Locate and identify every blood parasite.
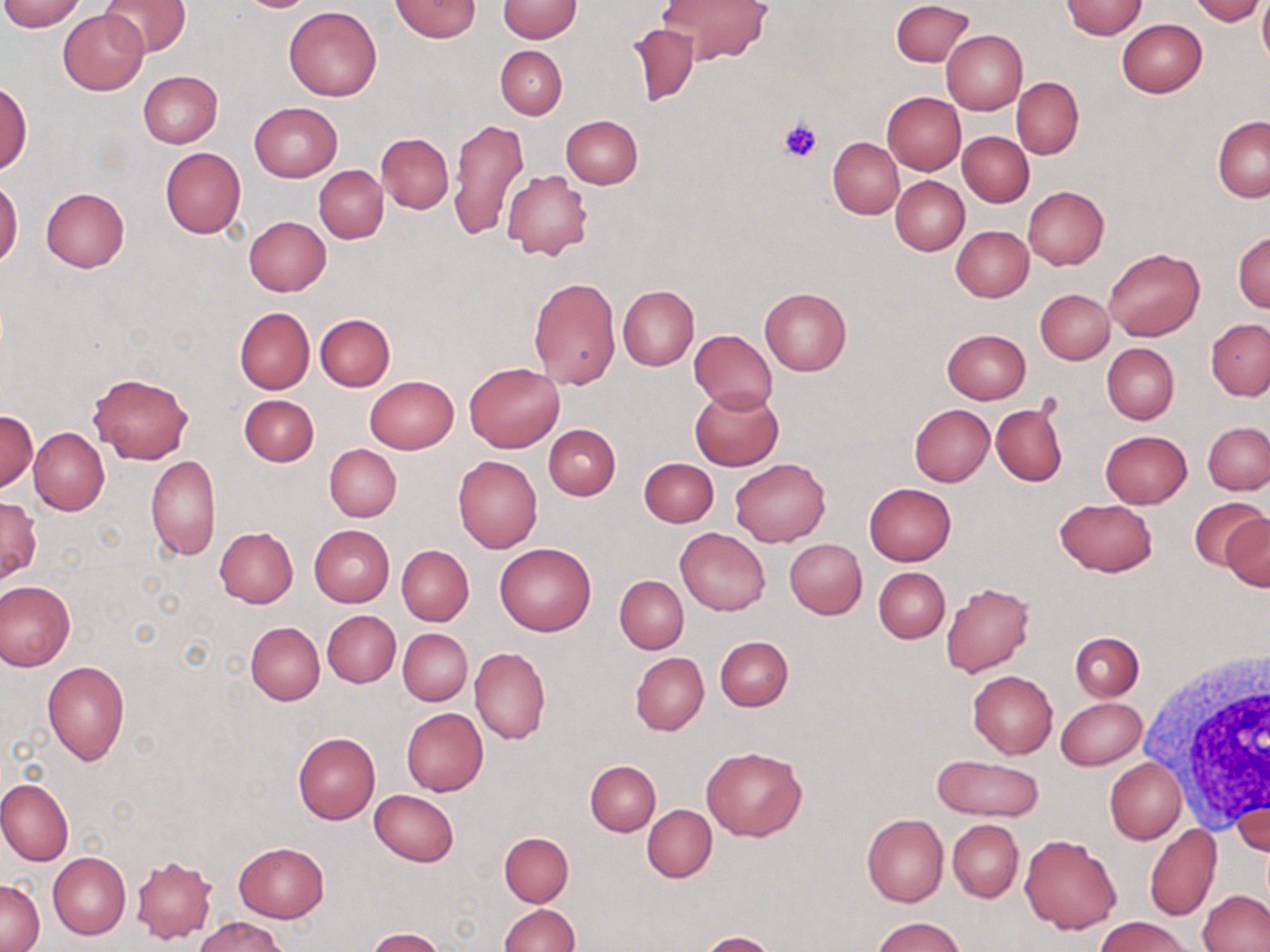

No blood parasites seen.

Approximate bounding boxes as [x1, y1, x2, y2] in pixels. White blood cell locations: [1135, 648, 1270, 840]. Uninfected red blood cell locations: [0, 0, 86, 31], [99, 0, 191, 59], [391, 0, 481, 42], [498, 0, 581, 42], [660, 0, 770, 64], [892, 0, 973, 67], [1061, 0, 1147, 39], [1190, 0, 1264, 24], [1258, 0, 1270, 67], [284, 6, 382, 101], [59, 9, 148, 94], [1117, 19, 1206, 97], [626, 23, 700, 107], [942, 30, 1028, 115], [496, 46, 567, 119], [138, 71, 223, 148], [1012, 76, 1084, 159], [1, 83, 32, 173], [882, 91, 966, 174], [249, 102, 343, 182], [560, 115, 642, 189], [1212, 116, 1270, 201], [448, 118, 530, 241], [957, 131, 1034, 207], [377, 132, 453, 213], [829, 138, 904, 219], [160, 147, 245, 239], [315, 165, 388, 243], [502, 170, 593, 261], [891, 176, 969, 255], [0, 179, 23, 267], [1023, 185, 1108, 270], [40, 186, 129, 273], [243, 216, 330, 296], [950, 225, 1034, 301], [1233, 232, 1270, 313], [1104, 246, 1204, 341], [529, 277, 621, 388], [617, 285, 699, 371], [760, 288, 852, 376], [1036, 289, 1114, 364], [234, 307, 314, 393], [315, 314, 395, 392], [1206, 319, 1270, 400], [941, 328, 1031, 404], [689, 330, 777, 412], [1101, 343, 1178, 424], [464, 362, 564, 452], [89, 372, 192, 463], [365, 375, 458, 453], [689, 388, 783, 471], [239, 394, 318, 467], [909, 403, 995, 486], [991, 403, 1067, 486], [1, 411, 37, 491], [1203, 421, 1270, 494], [544, 424, 621, 500], [29, 428, 109, 515], [1100, 430, 1193, 508], [324, 444, 401, 521], [147, 455, 221, 560], [453, 455, 542, 553], [639, 457, 718, 527], [730, 459, 831, 547], [864, 482, 955, 565], [0, 496, 42, 583], [1188, 497, 1266, 577], [1054, 499, 1157, 576], [1222, 512, 1270, 591], [309, 525, 395, 607], [214, 527, 298, 607], [675, 528, 769, 616], [786, 539, 866, 618], [494, 542, 596, 636], [397, 545, 474, 625], [873, 566, 949, 642], [615, 575, 688, 654], [0, 581, 75, 670], [942, 582, 1034, 678], [322, 610, 400, 687], [245, 622, 324, 705], [398, 629, 471, 705], [1070, 632, 1143, 701], [716, 635, 793, 710], [470, 648, 550, 744], [630, 652, 709, 735], [42, 660, 130, 767], [968, 669, 1057, 758], [951, 673, 1047, 823], [1055, 696, 1146, 770], [401, 708, 489, 796], [293, 732, 380, 824], [702, 746, 806, 840], [931, 754, 1044, 821], [1105, 757, 1186, 844], [585, 760, 661, 835], [0, 778, 73, 865], [370, 790, 458, 867], [1232, 794, 1269, 858], [642, 806, 716, 882], [862, 813, 948, 906], [949, 819, 1023, 902], [1144, 823, 1221, 920], [499, 832, 573, 906], [1019, 834, 1121, 934], [234, 842, 329, 923], [48, 852, 130, 939], [131, 854, 218, 943], [1, 877, 43, 951], [1199, 890, 1270, 951], [499, 904, 578, 952], [1097, 915, 1192, 951], [195, 916, 287, 952], [874, 917, 965, 952], [366, 928, 445, 952], [700, 931, 776, 952]. Platelet locations: [779, 116, 824, 161]. Slide-level diagnosis: negative for blood parasites. Image is 1270×952 pixels. 1000x magnification. May-Grünwald-Giemsa-stained preparation. Optical microscopy. One field of a larger specimen. Thin blood smear.